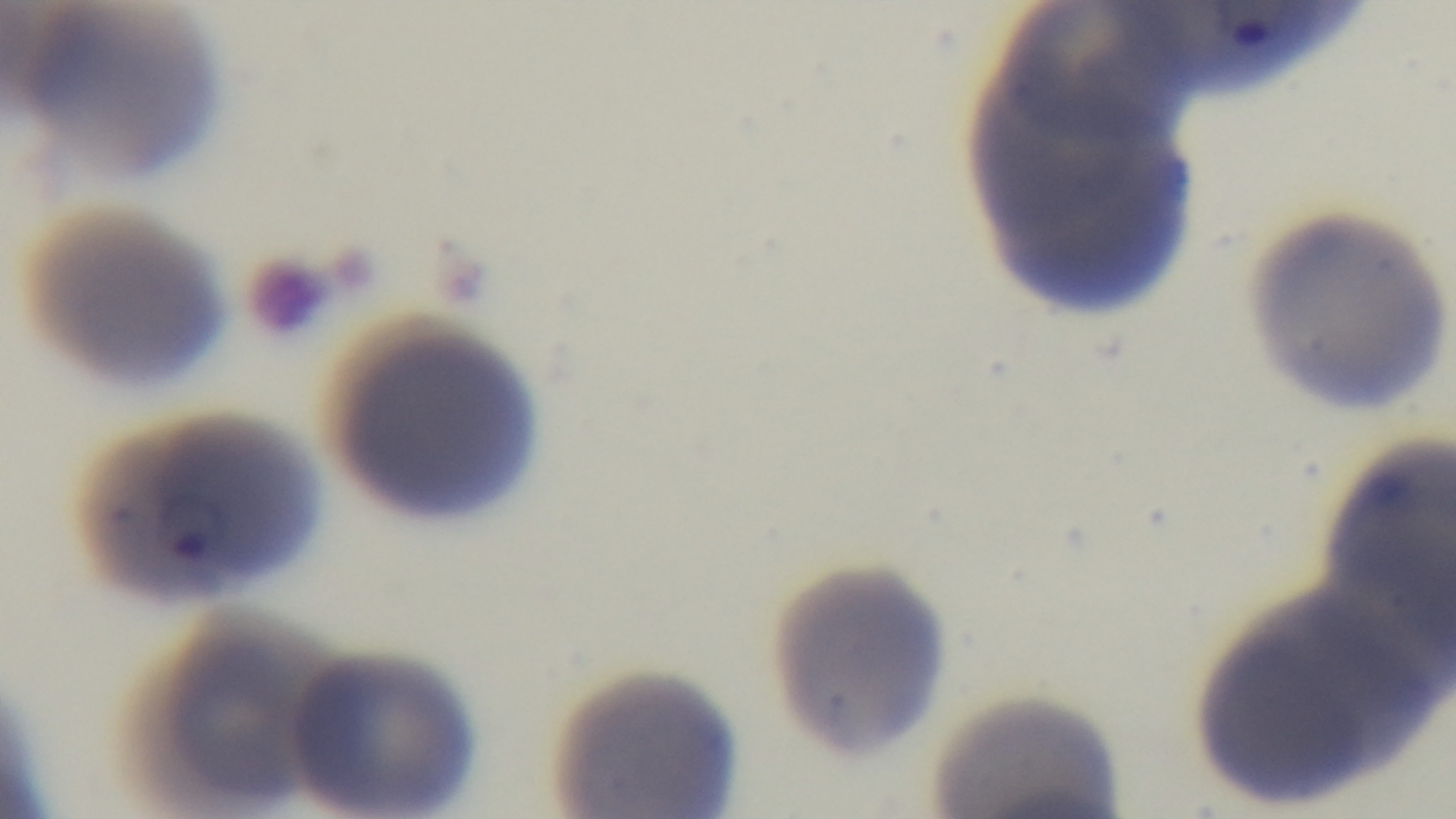

Single field of view. Giemsa stain. Preparation: thin blood film. Malaria status: infected. 100x oil-immersion objective. Captured with a mounted 4K digital camera. Light microscopy.